Name the cell type shown.
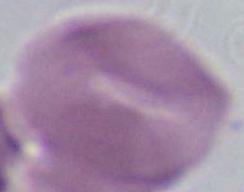
This is an erythrocyte.

Summary:
  - Modality: photomicrograph
  - Magnification: 1000x